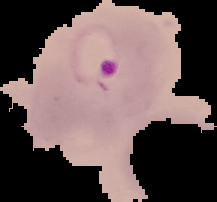
{
  "preparation": "thin blood film",
  "image_size": "217×202 pixels",
  "result": "Plasmodium parasites identified",
  "image_type": "cell region segmented out of the field of view; surrounding area masked to black"
}